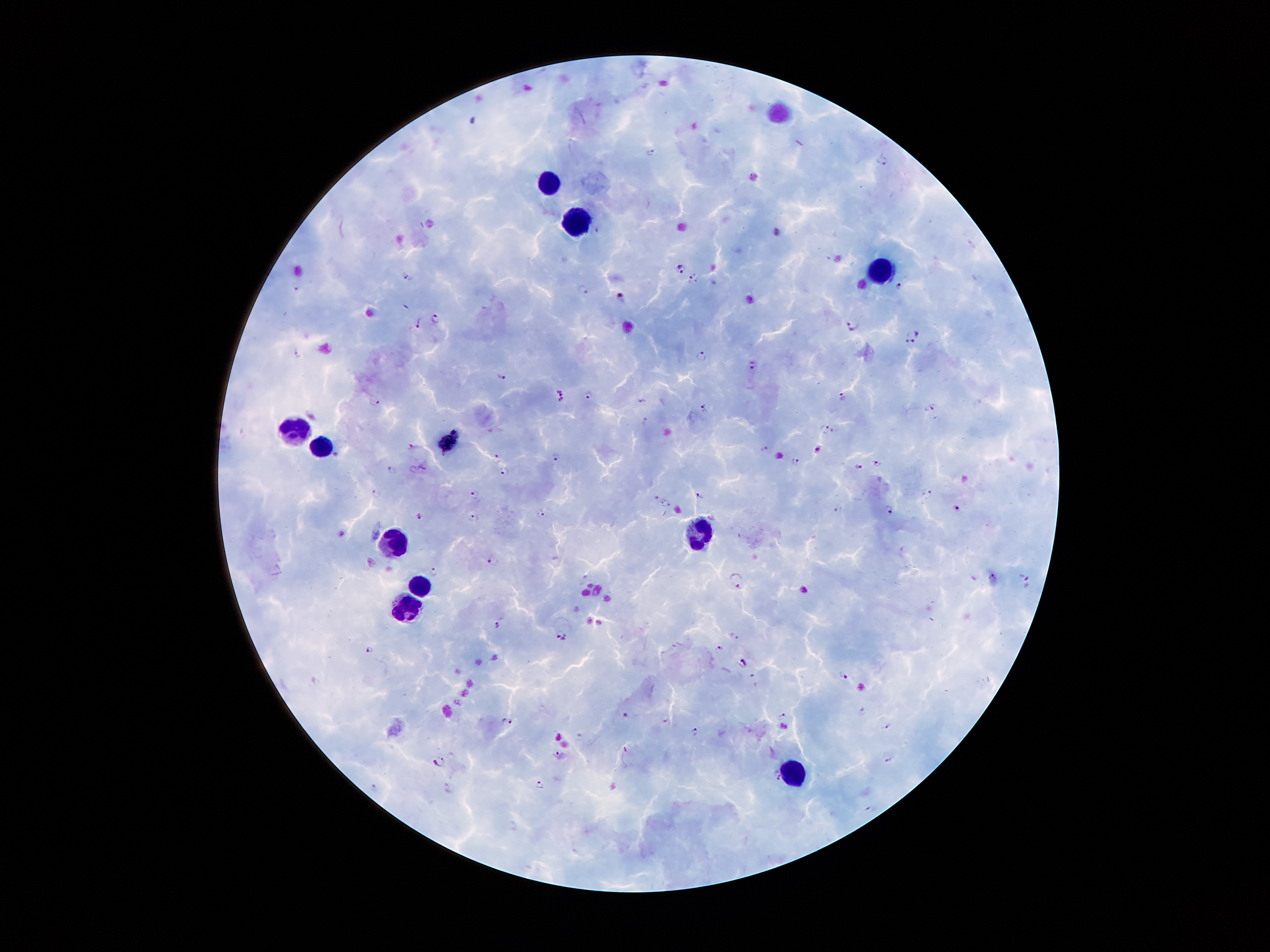
malaria_parasite_locations: 'approximate centers as [x, y] in pixels: [650, 151], [885, 160], [680, 267], [407, 278], [693, 279], [898, 285], [296, 288], [583, 290], [621, 296], [435, 320], [418, 322], [854, 323], [911, 336], [297, 352], [701, 356], [752, 365], [500, 376], [588, 393], [561, 395], [841, 395], [642, 401], [375, 402], [704, 407], [930, 407], [824, 428], [412, 445], [764, 449], [817, 450], [556, 455], [496, 457], [795, 461], [877, 463], [423, 467], [858, 467], [392, 470], [505, 471], [377, 493], [927, 494], [474, 495], [700, 496], [665, 503], [838, 509], [890, 509], [957, 509], [541, 514], [419, 515], [473, 518], [494, 561], [433, 572], [993, 578], [736, 579], [1027, 580], [497, 624], [562, 637], [719, 649], [371, 650], [744, 663], [844, 674], [863, 711], [626, 716], [781, 717], [509, 721], [885, 726], [694, 731], [560, 755], [888, 756], [439, 761], [776, 774], [541, 782], [373, 787], [869, 808]'
image_size: 1270×952 pixels
patient_malaria_status: positive for Plasmodium falciparum
magnification: 100x
stain: Giemsa
capture: smartphone camera through the microscope eyepiece
preparation: thick peripheral-blood smear
field_of_view: one from this slide
leukocyte_locations: 'approximate centers as [x, y] in pixels: [551, 184], [578, 217], [880, 268], [293, 427], [451, 442], [322, 448], [700, 531], [401, 545], [419, 582], [405, 611], [796, 777]'